Locate and identify every blood parasite.
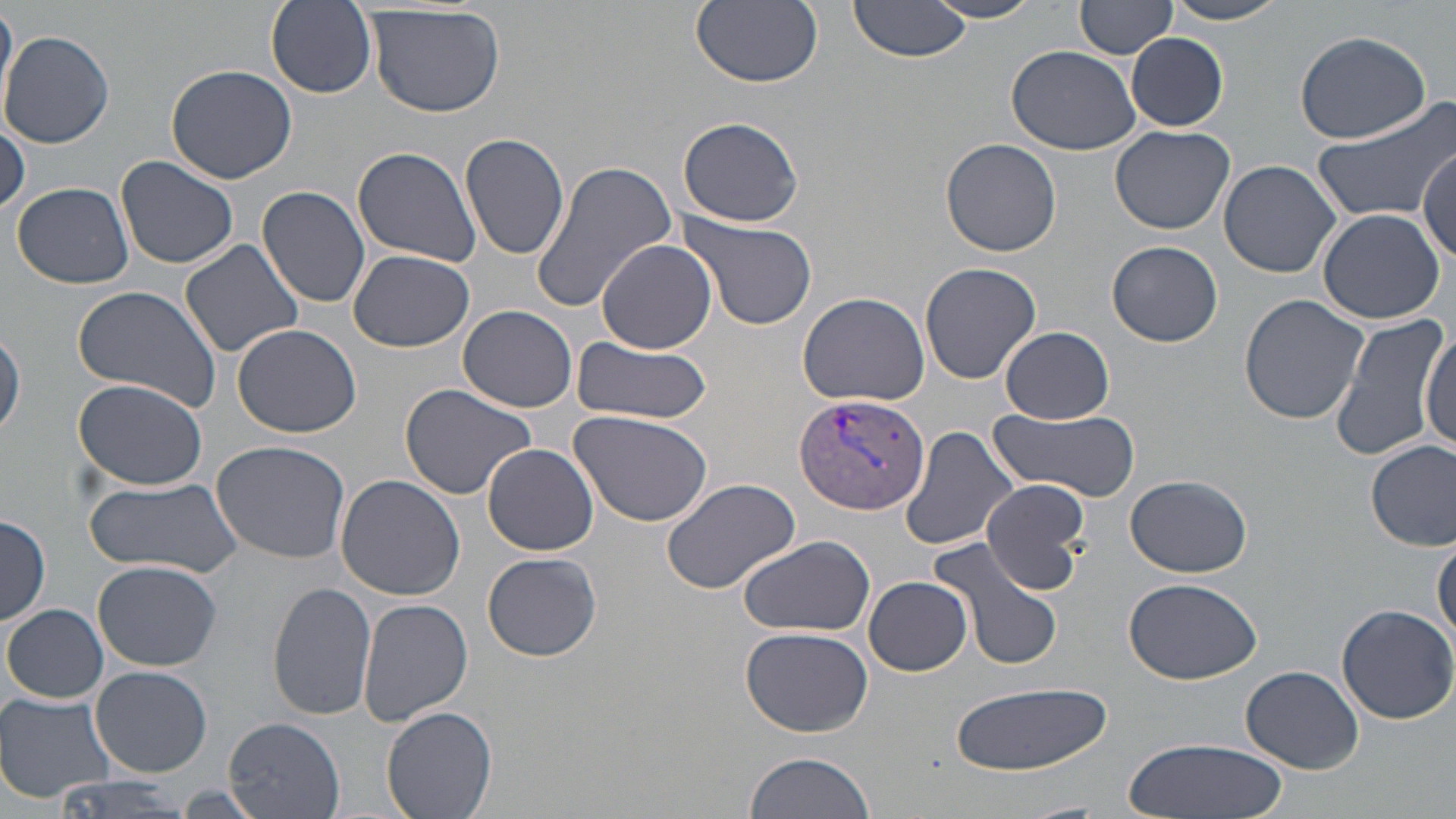

Approximate bounding boxes as (x1, y1, x2, y2) in pixels.
Plasmodium vivax-infected red blood cells: (796, 394, 932, 516).
No Plasmodium falciparum, Plasmodium ovale, Plasmodium malariae, Babesia divergens, or Trypanosoma brucei observed.

Summary:
  - Uninfected red blood cell locations: (265, 0, 378, 99), (690, 0, 822, 88), (851, 0, 974, 60), (928, 0, 1048, 24), (1078, 0, 1178, 59), (0, 1, 17, 115), (1159, 1, 1298, 26), (367, 4, 506, 118), (1, 29, 118, 148), (1293, 30, 1433, 144), (1128, 32, 1229, 129), (1007, 44, 1140, 155), (164, 64, 297, 184), (1312, 97, 1456, 224), (677, 116, 806, 228), (0, 118, 28, 216), (1110, 125, 1234, 235), (459, 132, 570, 260), (940, 137, 1063, 256), (1418, 144, 1454, 258), (353, 146, 481, 267), (117, 156, 239, 271), (1218, 159, 1342, 278), (532, 161, 680, 314), (11, 182, 135, 289), (258, 185, 371, 308), (1316, 207, 1446, 324), (676, 211, 818, 331), (179, 238, 304, 358), (596, 239, 716, 353), (1107, 240, 1222, 348), (346, 250, 477, 352), (920, 261, 1041, 385), (70, 285, 224, 413), (799, 292, 928, 405), (1239, 294, 1370, 426), (459, 305, 580, 413), (1328, 310, 1451, 463), (232, 323, 362, 438), (1, 325, 24, 443), (999, 326, 1116, 423), (1418, 328, 1456, 456), (571, 336, 712, 423), (73, 380, 208, 491), (398, 383, 538, 501), (569, 409, 715, 528), (990, 409, 1140, 499), (901, 427, 1020, 554), (1367, 439, 1455, 551), (210, 440, 353, 566), (482, 442, 599, 555), (1126, 473, 1253, 578), (83, 475, 243, 579), (335, 475, 466, 600), (659, 476, 802, 594), (979, 478, 1091, 592), (0, 511, 49, 629), (1432, 533, 1456, 647), (737, 534, 876, 638), (927, 535, 1065, 672), (483, 551, 602, 661), (92, 560, 222, 670), (862, 576, 973, 676), (1123, 577, 1262, 684), (268, 582, 377, 721), (359, 600, 473, 727), (1337, 603, 1455, 722), (3, 604, 108, 703), (739, 626, 875, 738), (90, 666, 214, 777), (1241, 666, 1366, 775), (945, 682, 1112, 775), (0, 694, 116, 805), (383, 705, 497, 819), (224, 718, 344, 817), (1121, 736, 1288, 819), (742, 751, 878, 819), (51, 775, 195, 819)
  - Slide-level diagnosis: Plasmodium vivax
  - Magnification: 1000x
  - Preparation: thin blood film
  - Modality: light microscopy
  - Field of view: one of a larger specimen
  - Stain: May-Grünwald-Giemsa
  - Image size: 1456×819 pixels